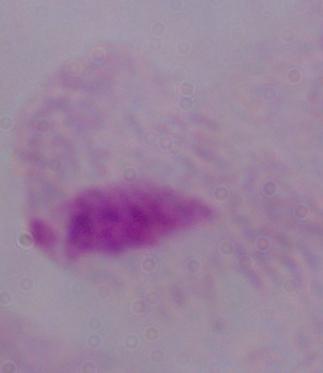
Summary:
  - Identification: trichomonad
  - Modality: micrograph
  - Magnification: 1000x